Identify the parasite.
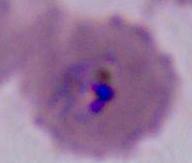
This is Plasmodium.

Summary:
  - Modality: photomicrograph
  - Magnification: 400x or 1000x